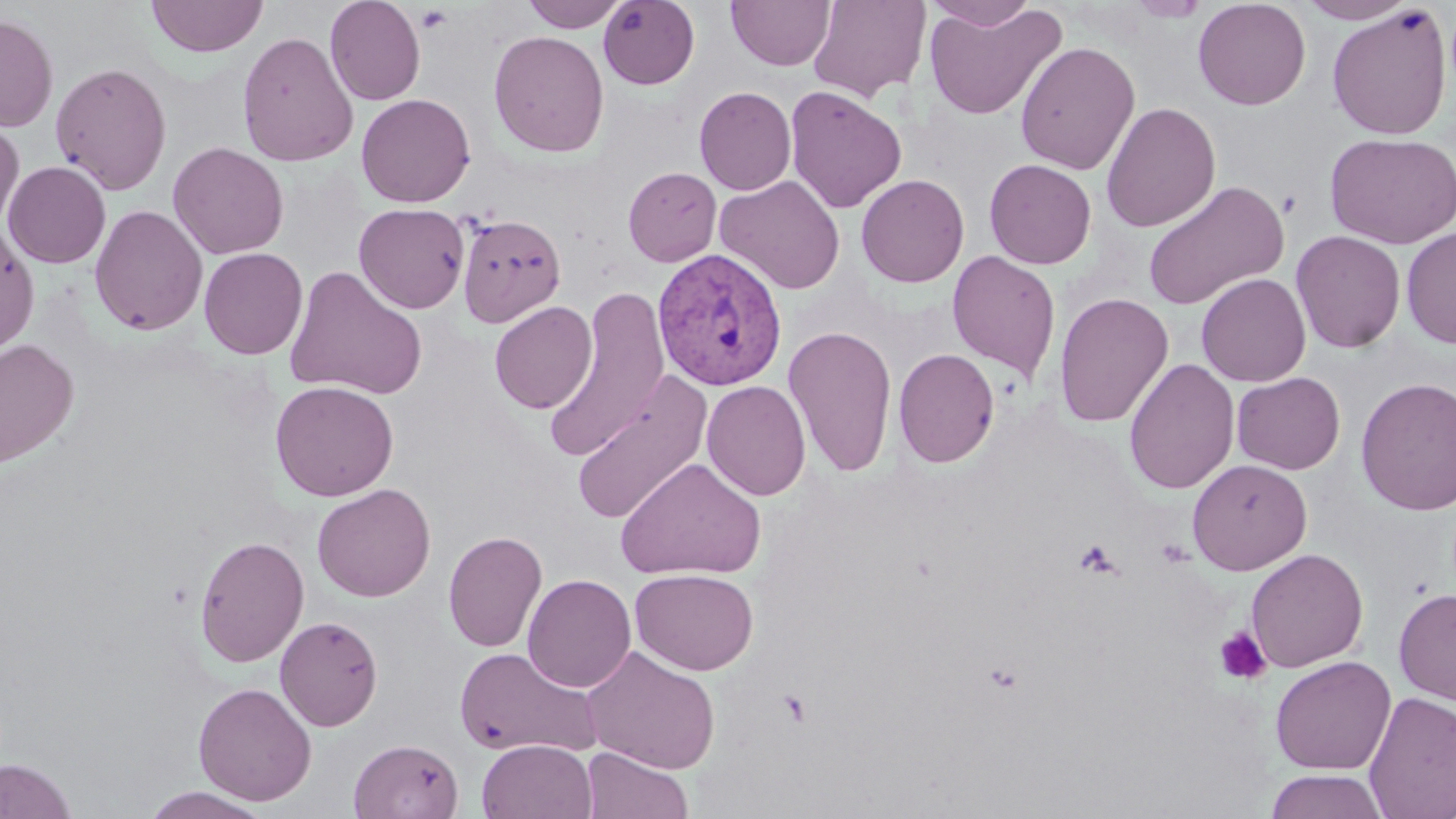
slide-level diagnosis = Plasmodium vivax
image size = 1456×819 pixels
modality = light microscopy
magnification = 1000x
uninfected red blood cell locations = approximate bounding boxes as [x1, y1, x2, y2] in pixels: [146, 0, 268, 58], [325, 0, 425, 106], [726, 0, 836, 70], [808, 0, 931, 102], [924, 0, 1040, 30], [1126, 0, 1209, 22], [1192, 0, 1311, 110], [1297, 0, 1415, 24], [523, 1, 628, 31], [598, 1, 700, 89], [923, 4, 1067, 120], [1327, 5, 1452, 140], [0, 13, 58, 132], [488, 30, 610, 158], [236, 31, 358, 167], [1015, 41, 1140, 175], [50, 61, 173, 195], [784, 84, 907, 214], [694, 86, 797, 195], [356, 93, 476, 207], [1100, 102, 1221, 233], [0, 120, 24, 232], [1325, 132, 1456, 249], [168, 141, 289, 260], [983, 158, 1097, 269], [3, 160, 111, 269], [623, 167, 722, 266], [856, 173, 970, 288], [714, 175, 846, 294], [1143, 180, 1289, 311], [354, 203, 470, 314], [89, 204, 208, 336], [456, 213, 566, 327], [0, 222, 39, 357], [1401, 226, 1456, 348], [1291, 231, 1406, 353], [199, 247, 308, 359], [946, 251, 1061, 382], [283, 265, 428, 401], [1196, 273, 1311, 387], [542, 289, 670, 462], [1053, 292, 1174, 428], [489, 301, 597, 413], [784, 325, 898, 477], [0, 338, 79, 468], [893, 348, 1000, 468], [1123, 357, 1239, 494], [571, 372, 714, 527], [1232, 372, 1346, 474], [1355, 377, 1456, 516], [270, 380, 399, 501], [701, 380, 811, 501], [616, 456, 767, 582], [1188, 459, 1312, 575], [312, 483, 436, 602], [442, 530, 547, 653], [193, 534, 309, 668], [1245, 548, 1368, 672], [629, 568, 759, 675], [522, 573, 637, 693], [1393, 588, 1456, 706], [275, 616, 383, 731], [453, 646, 601, 759], [581, 646, 721, 774], [1269, 655, 1396, 774], [193, 682, 317, 806], [1362, 691, 1456, 818], [348, 738, 464, 819], [476, 739, 597, 819], [581, 747, 693, 819], [1, 758, 78, 818], [1263, 769, 1391, 819], [140, 787, 274, 819]
preparation = thin blood smear
field of view = single
platelet locations = approximate bounding boxes as [x1, y1, x2, y2] in pixels: [415, 5, 453, 34], [1277, 189, 1303, 218], [1073, 538, 1121, 578], [1213, 627, 1272, 685]
Plasmodium vivax-infected red blood cell locations = approximate bounding boxes as [x1, y1, x2, y2] in pixels: [651, 247, 787, 390]
stain = May-Grünwald-Giemsa